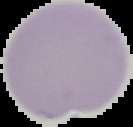
malaria status = uninfected
preparation = thin blood film
image type = segmented cell region with the area outside set to black
image size = 133×127 pixels